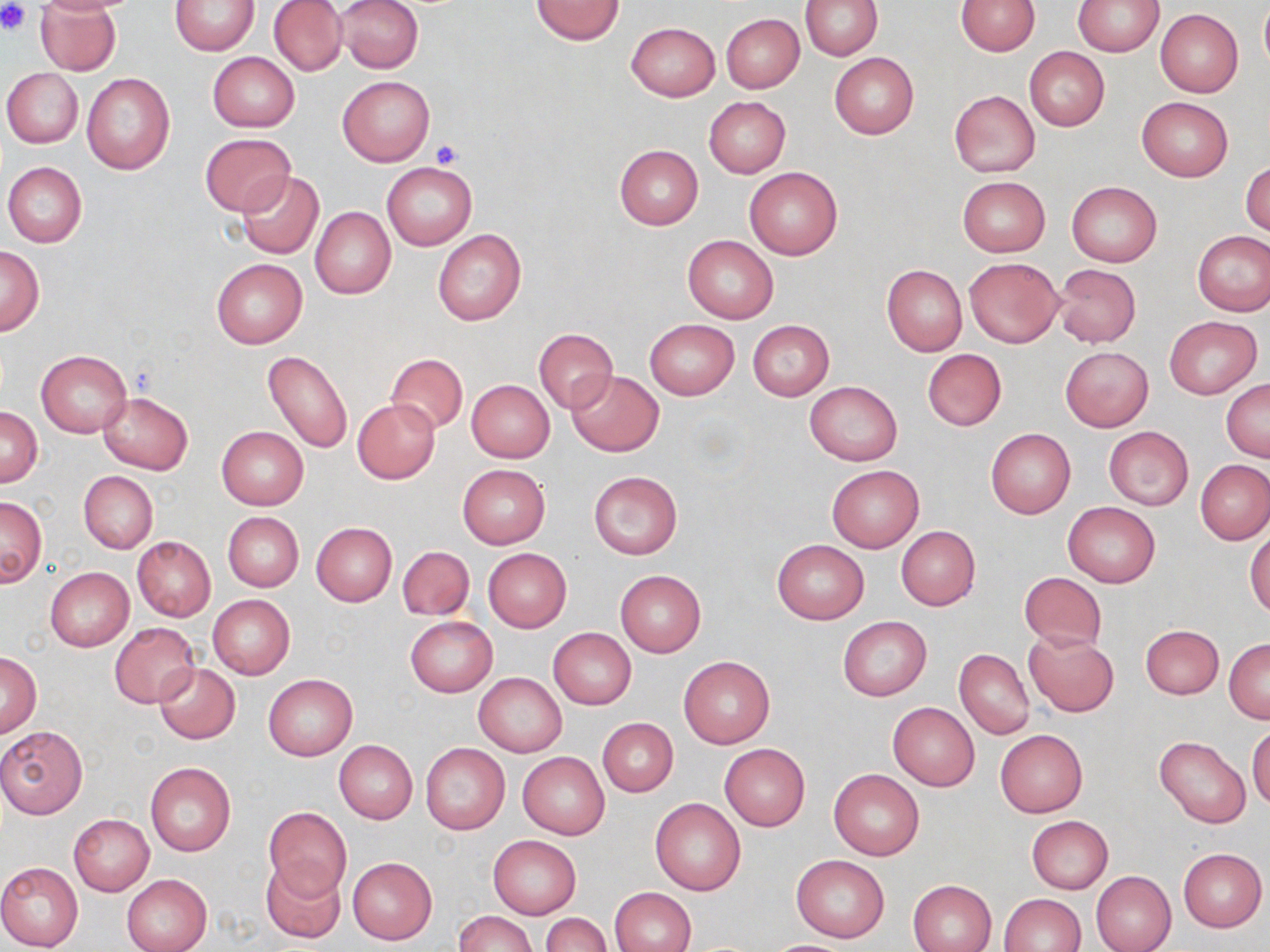
slide_level_diagnosis: no evidence of blood parasites
magnification: 1000x
preparation: thin blood film
stain: May-Grünwald-Giemsa
field_of_view: one of a larger specimen
image_size: 1270×952 pixels
uninfected_red_blood_cell_locations: 'approximate bounding boxes as named x1/y1/x2/y2 corners in pixels: (x1=35, y1=0, x2=121, y2=75), (x1=269, y1=0, x2=347, y2=76), (x1=337, y1=0, x2=423, y2=74), (x1=531, y1=0, x2=624, y2=45), (x1=800, y1=0, x2=882, y2=60), (x1=957, y1=0, x2=1040, y2=55), (x1=170, y1=1, x2=259, y2=55), (x1=1075, y1=1, x2=1163, y2=55), (x1=1259, y1=2, x2=1270, y2=73), (x1=1155, y1=9, x2=1242, y2=96), (x1=721, y1=14, x2=804, y2=92), (x1=626, y1=21, x2=720, y2=100), (x1=1024, y1=46, x2=1110, y2=132), (x1=829, y1=52, x2=919, y2=138), (x1=207, y1=53, x2=299, y2=132), (x1=2, y1=68, x2=83, y2=149), (x1=81, y1=73, x2=175, y2=174), (x1=337, y1=76, x2=435, y2=166), (x1=948, y1=90, x2=1040, y2=177), (x1=703, y1=96, x2=791, y2=177), (x1=1136, y1=97, x2=1234, y2=181), (x1=200, y1=134, x2=297, y2=216), (x1=613, y1=144, x2=704, y2=229), (x1=1241, y1=159, x2=1269, y2=239), (x1=2, y1=162, x2=88, y2=247), (x1=382, y1=162, x2=476, y2=249), (x1=744, y1=167, x2=842, y2=259), (x1=236, y1=171, x2=325, y2=259), (x1=957, y1=176, x2=1050, y2=257), (x1=1066, y1=181, x2=1161, y2=268), (x1=310, y1=206, x2=397, y2=299), (x1=432, y1=229, x2=526, y2=326), (x1=1193, y1=230, x2=1270, y2=317), (x1=683, y1=235, x2=778, y2=324), (x1=0, y1=246, x2=44, y2=336), (x1=211, y1=258, x2=307, y2=348), (x1=965, y1=258, x2=1063, y2=347), (x1=1052, y1=263, x2=1141, y2=348), (x1=881, y1=265, x2=967, y2=356), (x1=1163, y1=315, x2=1262, y2=399), (x1=645, y1=319, x2=739, y2=399), (x1=748, y1=320, x2=834, y2=400), (x1=533, y1=328, x2=617, y2=413), (x1=1060, y1=347, x2=1153, y2=431), (x1=922, y1=348, x2=1007, y2=431), (x1=37, y1=349, x2=131, y2=437), (x1=261, y1=350, x2=353, y2=455), (x1=387, y1=353, x2=468, y2=434), (x1=566, y1=370, x2=664, y2=455), (x1=1222, y1=377, x2=1270, y2=461), (x1=467, y1=379, x2=555, y2=463), (x1=805, y1=381, x2=902, y2=465), (x1=98, y1=393, x2=193, y2=474), (x1=353, y1=399, x2=441, y2=483), (x1=1, y1=408, x2=42, y2=486), (x1=217, y1=426, x2=308, y2=509), (x1=1103, y1=426, x2=1193, y2=510), (x1=985, y1=428, x2=1076, y2=518), (x1=1196, y1=459, x2=1270, y2=544), (x1=457, y1=464, x2=550, y2=548), (x1=826, y1=465, x2=924, y2=551), (x1=589, y1=470, x2=683, y2=560), (x1=78, y1=471, x2=157, y2=552), (x1=0, y1=496, x2=48, y2=588), (x1=1063, y1=501, x2=1160, y2=587), (x1=222, y1=512, x2=304, y2=592), (x1=311, y1=522, x2=396, y2=606), (x1=896, y1=526, x2=981, y2=610), (x1=1247, y1=529, x2=1270, y2=618), (x1=133, y1=536, x2=215, y2=621), (x1=772, y1=539, x2=868, y2=624), (x1=397, y1=546, x2=475, y2=621), (x1=483, y1=548, x2=571, y2=632), (x1=45, y1=567, x2=134, y2=651), (x1=615, y1=570, x2=706, y2=656), (x1=1018, y1=571, x2=1107, y2=651), (x1=207, y1=595, x2=295, y2=680), (x1=837, y1=616, x2=932, y2=701), (x1=405, y1=617, x2=497, y2=696), (x1=109, y1=622, x2=200, y2=707), (x1=1139, y1=625, x2=1223, y2=699), (x1=548, y1=628, x2=635, y2=710), (x1=1023, y1=631, x2=1119, y2=717), (x1=1224, y1=638, x2=1270, y2=722), (x1=954, y1=649, x2=1034, y2=739), (x1=1, y1=652, x2=41, y2=737), (x1=679, y1=655, x2=775, y2=748), (x1=154, y1=662, x2=240, y2=744), (x1=474, y1=673, x2=567, y2=757), (x1=263, y1=674, x2=357, y2=760), (x1=887, y1=702, x2=980, y2=790), (x1=599, y1=718, x2=678, y2=796), (x1=0, y1=725, x2=88, y2=818), (x1=1247, y1=725, x2=1270, y2=810), (x1=995, y1=729, x2=1087, y2=816), (x1=1154, y1=736, x2=1251, y2=829), (x1=334, y1=741, x2=417, y2=823), (x1=420, y1=743, x2=510, y2=835), (x1=719, y1=744, x2=810, y2=831), (x1=517, y1=752, x2=610, y2=840), (x1=145, y1=762, x2=235, y2=856), (x1=829, y1=769, x2=924, y2=860), (x1=651, y1=798, x2=746, y2=895), (x1=262, y1=807, x2=352, y2=901), (x1=69, y1=814, x2=155, y2=895), (x1=1026, y1=816, x2=1113, y2=893), (x1=488, y1=836, x2=580, y2=918), (x1=1178, y1=847, x2=1267, y2=931), (x1=791, y1=854, x2=890, y2=942), (x1=347, y1=856, x2=437, y2=944), (x1=260, y1=859, x2=346, y2=944), (x1=0, y1=861, x2=83, y2=952), (x1=1090, y1=871, x2=1176, y2=952), (x1=122, y1=874, x2=212, y2=952), (x1=908, y1=880, x2=996, y2=952), (x1=611, y1=887, x2=696, y2=952), (x1=1000, y1=893, x2=1086, y2=952), (x1=454, y1=911, x2=537, y2=952), (x1=541, y1=913, x2=611, y2=952), (x1=761, y1=939, x2=858, y2=951)'
modality: light microscopy
platelet_locations: 'approximate bounding boxes as named x1/y1/x2/y2 corners in pixels: (x1=0, y1=1, x2=30, y2=36), (x1=430, y1=140, x2=461, y2=168)'